Comment on the morphology of the red blood cells.
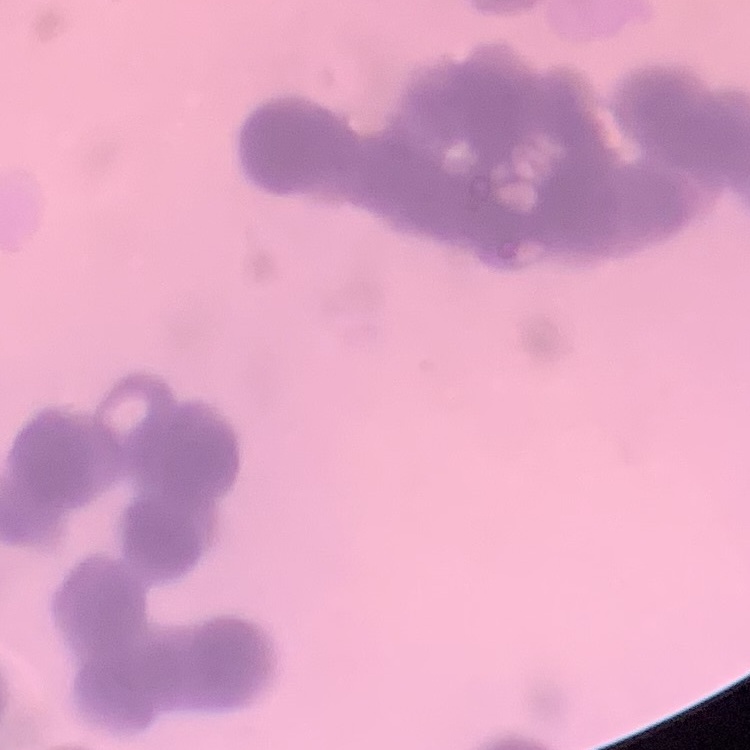
They show rouleaux formation.

stain = Field's or Giemsa
preparation = thin blood smear
image type = one tile cut from a larger photomicrograph